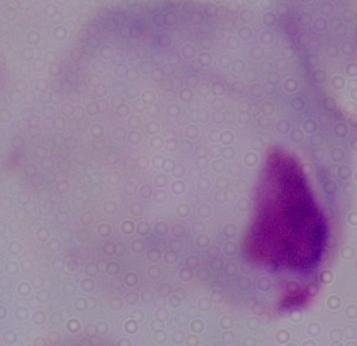

Summary:
  - Modality: micrograph
  - Identification: trichomonad
  - Magnification: 1000x